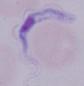
Summary:
  - Magnification: 1000x
  - Identification: trypanosome
  - Modality: photomicrograph